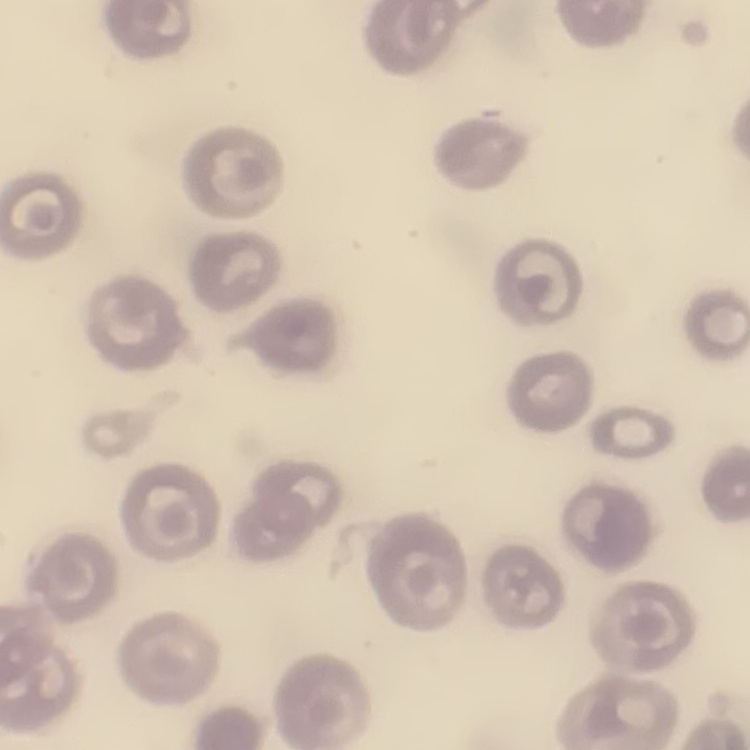
Summary:
  - Red blood cell morphology: no rouleaux formation
  - Preparation: thin blood film
  - Image type: square crop of a larger photomicrograph
  - Stain: Field's or Giemsa